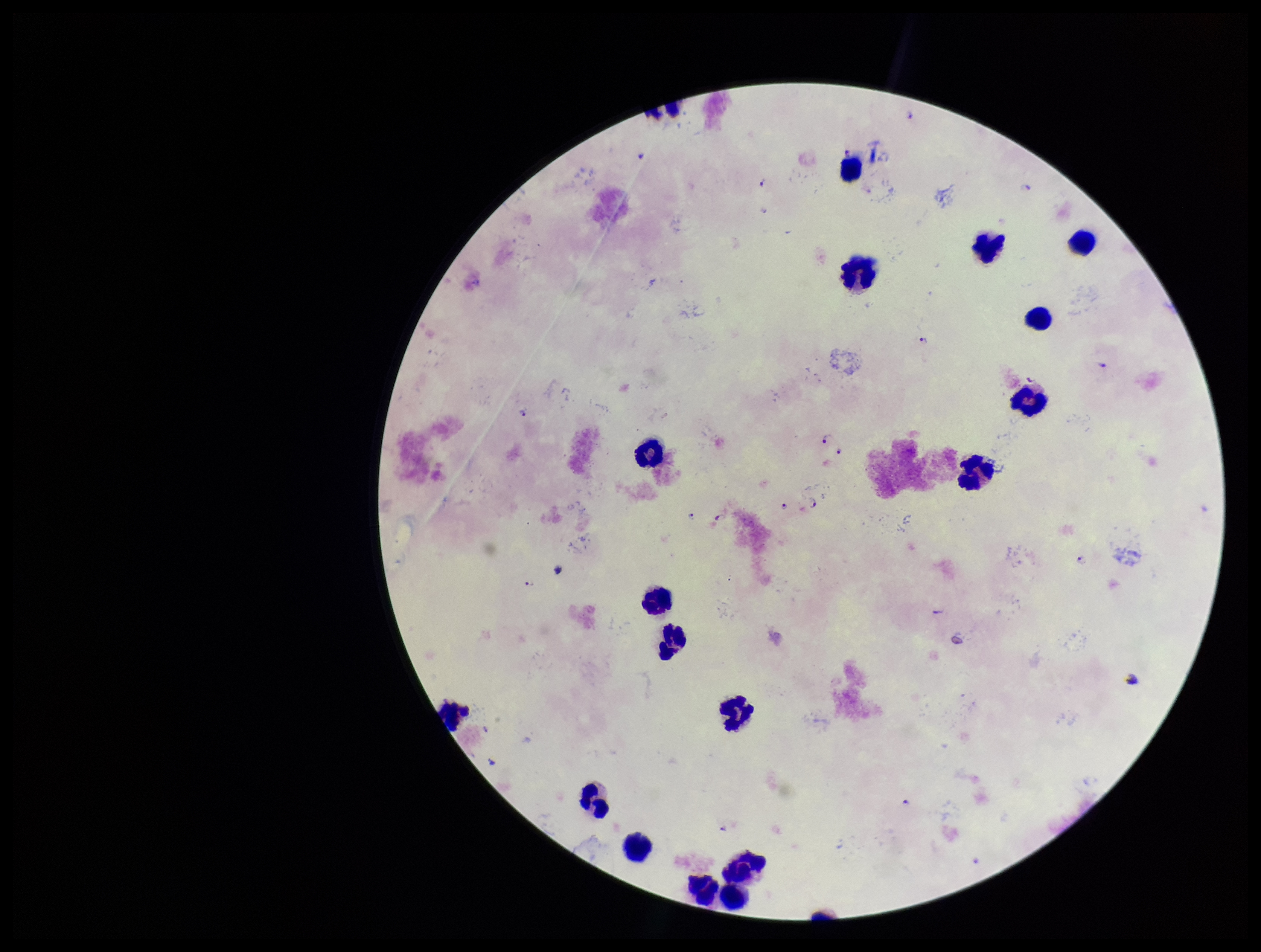
leukocyte count = 17
parasite count = 18
image size = 1261×952 pixels
preparation = thick
species reported for this patient = Plasmodium falciparum
Plasmodium parasites = seen
patient malaria status = positive
field of view = single
capture = smartphone photograph through the microscope eyepiece
stain = Giemsa